Give the extent of all Plasmodium ovale-infected red blood cells.
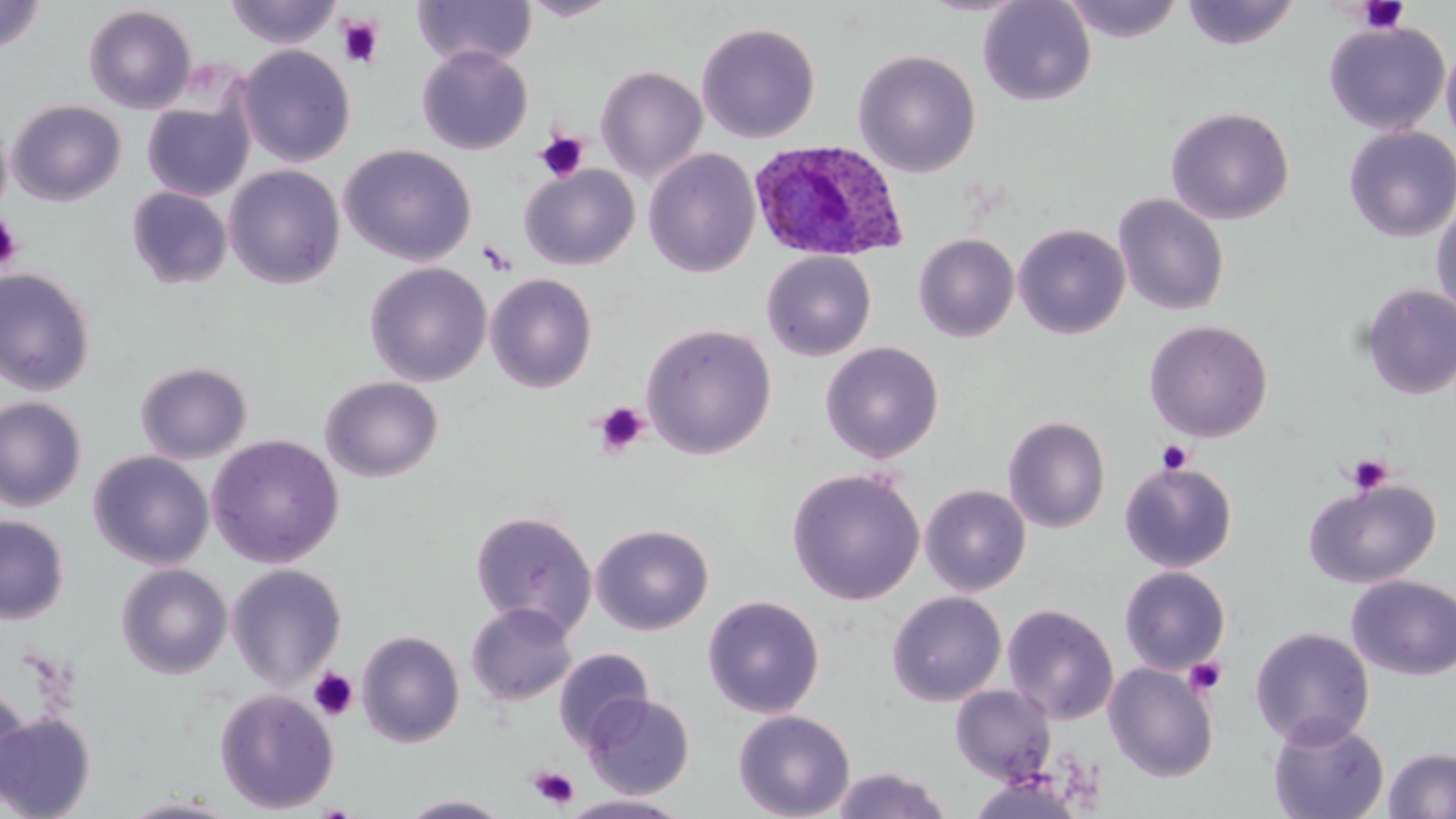

Approximate bounding boxes as [x1, y1, x2, y2] in pixels.
Plasmodium ovale-infected red blood cells: [748, 138, 909, 263].

Summary:
  - Platelet locations: [1356, 1, 1410, 33], [337, 16, 384, 68], [535, 131, 589, 182], [0, 212, 23, 274], [477, 239, 516, 274], [592, 401, 650, 458], [1157, 441, 1193, 474], [1345, 453, 1393, 494], [1183, 657, 1227, 695], [308, 667, 358, 721], [528, 766, 580, 809]
  - Uninfected red blood cell locations: [518, 0, 623, 21], [978, 0, 1097, 107], [1062, 0, 1186, 43], [1180, 0, 1301, 50], [0, 1, 47, 54], [224, 1, 343, 49], [412, 1, 537, 68], [83, 5, 197, 113], [1323, 20, 1450, 135], [696, 22, 820, 144], [1441, 39, 1456, 152], [237, 44, 356, 167], [417, 45, 533, 155], [853, 49, 981, 177], [595, 65, 708, 183], [142, 97, 253, 201], [7, 99, 126, 206], [1166, 107, 1295, 225], [1343, 125, 1456, 242], [339, 144, 477, 266], [643, 148, 760, 278], [520, 164, 640, 270], [224, 165, 345, 289], [127, 187, 232, 289], [1113, 194, 1230, 316], [1431, 201, 1456, 323], [1013, 223, 1130, 338], [914, 233, 1020, 342], [761, 251, 876, 361], [365, 262, 492, 387], [0, 268, 96, 395], [484, 272, 599, 393], [1359, 284, 1456, 400], [1144, 320, 1273, 443], [640, 323, 777, 459], [820, 341, 944, 463], [135, 361, 252, 464], [320, 375, 443, 483], [0, 396, 87, 511], [1003, 415, 1111, 533], [206, 434, 345, 568], [89, 450, 214, 570], [1119, 461, 1237, 572], [786, 467, 925, 605], [1304, 477, 1441, 588], [920, 485, 1031, 597], [470, 510, 598, 637], [0, 515, 69, 624], [591, 524, 714, 635], [116, 563, 233, 679], [226, 564, 347, 689], [1119, 566, 1231, 674], [1347, 574, 1456, 680], [887, 590, 1007, 706], [702, 595, 825, 718], [466, 603, 577, 707], [1002, 604, 1119, 724], [1250, 627, 1374, 749], [356, 631, 465, 747], [554, 647, 654, 749], [1103, 662, 1219, 782], [950, 684, 1056, 784], [0, 686, 32, 807], [214, 689, 339, 814], [582, 693, 695, 799], [733, 709, 855, 819], [0, 712, 97, 819], [1267, 717, 1389, 819], [1382, 747, 1456, 819], [831, 766, 953, 818], [969, 775, 1088, 819], [399, 793, 512, 818], [558, 793, 695, 819], [116, 796, 244, 818]
  - Slide-level diagnosis: Plasmodium ovale
  - Modality: optical microscopy
  - Field of view: single
  - Image size: 1456×819 pixels
  - Preparation: thin blood smear
  - Stain: May-Grünwald-Giemsa
  - Magnification: 1000x